State which parasite is depicted.
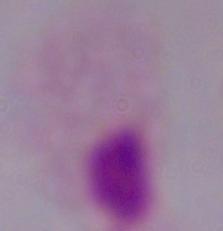

This is a trichomonad.

Summary:
  - Magnification: 1000x
  - Modality: micrograph